Classify this cell by malaria status.
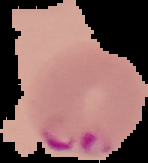
It is parasitized.

image size = 148×163 pixels
image type = cell region segmented out of the field of view; surrounding area masked to black
preparation = thin blood smear